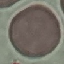
result = no malaria parasites detected
capture = smartphone through the microscope eyepiece
preparation = thin blood film
image type = cell patch, automatically extracted from a larger field of view and resized to 64 × 64 pixels
stain = Giemsa